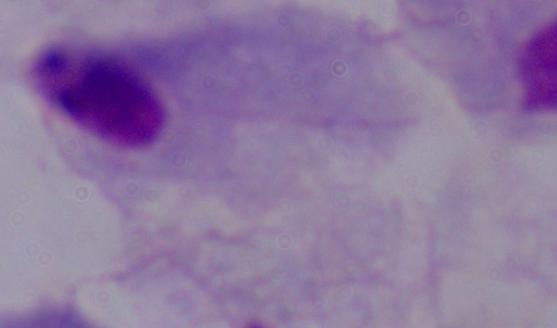
identification = trichomonad
modality = micrograph
magnification = 1000x